Describe the morphology of the erythrocytes.
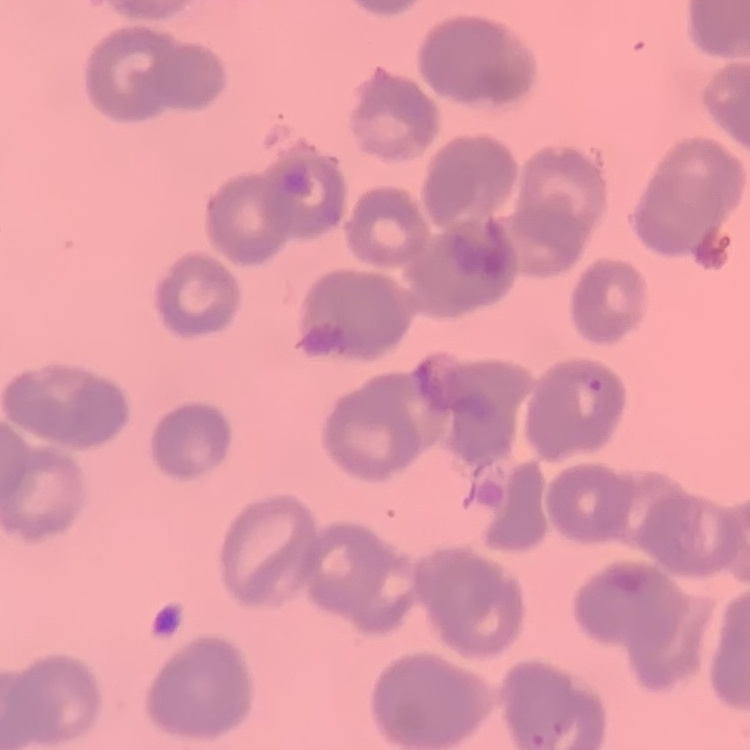
They show rouleaux formation.

Summary:
  - Preparation: thin blood smear
  - Stain: Field's or Giemsa
  - Image type: square crop of a larger photomicrograph